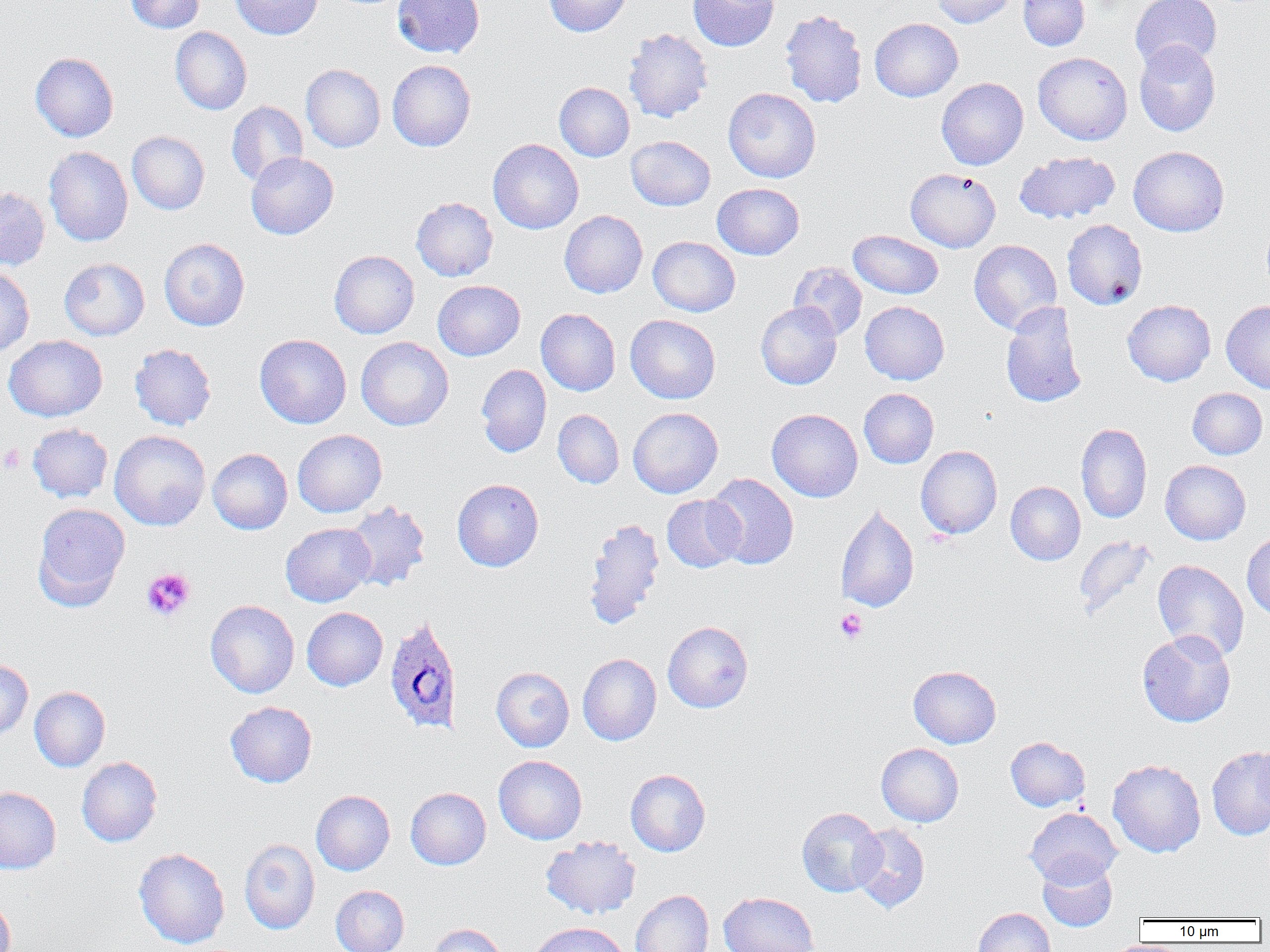

Summary:
  - Coordinate format: approximate bounding boxes as named x1/y1/x2/y2 corners in pixels
  - Uninfected red blood cell locations: (x1=125, y1=0, x2=204, y2=33), (x1=230, y1=0, x2=322, y2=40), (x1=392, y1=0, x2=485, y2=59), (x1=543, y1=0, x2=631, y2=37), (x1=688, y1=0, x2=779, y2=51), (x1=931, y1=0, x2=1016, y2=27), (x1=1018, y1=0, x2=1089, y2=51), (x1=1130, y1=0, x2=1222, y2=72), (x1=780, y1=9, x2=867, y2=108), (x1=870, y1=18, x2=963, y2=101), (x1=170, y1=27, x2=251, y2=115), (x1=623, y1=28, x2=713, y2=123), (x1=1134, y1=40, x2=1221, y2=136), (x1=30, y1=52, x2=119, y2=142), (x1=1033, y1=52, x2=1132, y2=145), (x1=387, y1=59, x2=476, y2=152), (x1=300, y1=64, x2=385, y2=152), (x1=936, y1=78, x2=1028, y2=170), (x1=554, y1=82, x2=634, y2=161), (x1=723, y1=87, x2=821, y2=183), (x1=227, y1=101, x2=307, y2=186), (x1=126, y1=131, x2=210, y2=215), (x1=626, y1=136, x2=715, y2=211), (x1=488, y1=138, x2=583, y2=234), (x1=44, y1=146, x2=133, y2=247), (x1=1128, y1=146, x2=1229, y2=237), (x1=1015, y1=151, x2=1119, y2=224), (x1=246, y1=152, x2=338, y2=239), (x1=905, y1=168, x2=1001, y2=252), (x1=712, y1=183, x2=804, y2=260), (x1=0, y1=187, x2=50, y2=270), (x1=411, y1=197, x2=498, y2=281), (x1=560, y1=210, x2=647, y2=297), (x1=1062, y1=219, x2=1147, y2=309), (x1=848, y1=229, x2=943, y2=299), (x1=648, y1=236, x2=740, y2=316), (x1=159, y1=238, x2=249, y2=331), (x1=969, y1=240, x2=1062, y2=334), (x1=329, y1=250, x2=419, y2=339), (x1=59, y1=258, x2=149, y2=340), (x1=789, y1=262, x2=868, y2=340), (x1=0, y1=267, x2=34, y2=357), (x1=433, y1=280, x2=525, y2=361), (x1=1122, y1=300, x2=1215, y2=386), (x1=755, y1=301, x2=841, y2=389), (x1=860, y1=301, x2=949, y2=384), (x1=1001, y1=301, x2=1087, y2=408), (x1=1221, y1=301, x2=1270, y2=393), (x1=536, y1=308, x2=620, y2=396), (x1=625, y1=314, x2=721, y2=403), (x1=255, y1=334, x2=351, y2=429), (x1=4, y1=335, x2=107, y2=421), (x1=356, y1=337, x2=453, y2=431), (x1=129, y1=343, x2=216, y2=430), (x1=476, y1=365, x2=551, y2=457), (x1=859, y1=388, x2=939, y2=468), (x1=1187, y1=388, x2=1267, y2=459), (x1=628, y1=407, x2=723, y2=498), (x1=553, y1=409, x2=624, y2=488), (x1=767, y1=409, x2=863, y2=502), (x1=1076, y1=422, x2=1152, y2=524), (x1=27, y1=423, x2=113, y2=502), (x1=292, y1=429, x2=387, y2=517), (x1=109, y1=430, x2=211, y2=531), (x1=916, y1=446, x2=1002, y2=539), (x1=207, y1=448, x2=292, y2=534), (x1=1161, y1=460, x2=1250, y2=545), (x1=705, y1=473, x2=799, y2=569), (x1=452, y1=479, x2=543, y2=571), (x1=1006, y1=482, x2=1085, y2=565), (x1=662, y1=495, x2=745, y2=572), (x1=343, y1=500, x2=430, y2=592), (x1=32, y1=503, x2=130, y2=610), (x1=835, y1=503, x2=919, y2=613), (x1=583, y1=517, x2=665, y2=629), (x1=281, y1=522, x2=375, y2=607), (x1=1242, y1=533, x2=1270, y2=620), (x1=1073, y1=534, x2=1157, y2=620), (x1=1153, y1=560, x2=1249, y2=661), (x1=205, y1=600, x2=299, y2=698), (x1=302, y1=607, x2=388, y2=691), (x1=663, y1=621, x2=753, y2=713), (x1=1137, y1=630, x2=1236, y2=727), (x1=577, y1=653, x2=661, y2=745), (x1=0, y1=658, x2=33, y2=740), (x1=908, y1=665, x2=1001, y2=748), (x1=491, y1=666, x2=574, y2=751), (x1=29, y1=686, x2=110, y2=771), (x1=225, y1=701, x2=317, y2=787), (x1=1005, y1=736, x2=1090, y2=812), (x1=876, y1=743, x2=963, y2=827), (x1=1207, y1=746, x2=1270, y2=840), (x1=493, y1=755, x2=587, y2=844), (x1=76, y1=756, x2=163, y2=847), (x1=1108, y1=759, x2=1206, y2=857), (x1=625, y1=769, x2=711, y2=856), (x1=0, y1=786, x2=61, y2=874), (x1=406, y1=788, x2=490, y2=870), (x1=311, y1=790, x2=394, y2=875), (x1=797, y1=807, x2=885, y2=897), (x1=1025, y1=808, x2=1122, y2=887), (x1=850, y1=824, x2=930, y2=913), (x1=541, y1=835, x2=641, y2=919), (x1=239, y1=839, x2=320, y2=934), (x1=133, y1=847, x2=230, y2=949), (x1=1037, y1=858, x2=1117, y2=931), (x1=330, y1=885, x2=409, y2=952), (x1=630, y1=890, x2=713, y2=952), (x1=718, y1=891, x2=819, y2=952), (x1=0, y1=893, x2=16, y2=952), (x1=973, y1=907, x2=1056, y2=952), (x1=528, y1=922, x2=631, y2=952), (x1=428, y1=923, x2=508, y2=952)
  - Platelet locations: (x1=0, y1=444, x2=26, y2=474), (x1=141, y1=567, x2=196, y2=621), (x1=835, y1=608, x2=868, y2=644)
  - Plasmodium ovale-infected red blood cell locations: (x1=383, y1=615, x2=463, y2=734)
  - Slide-level diagnosis: Plasmodium ovale
  - Image size: 1270×952 pixels
  - Modality: optical microscopy
  - Field of view: single
  - Preparation: thin blood smear
  - Magnification: 1000x